Report the malaria status of this cell.
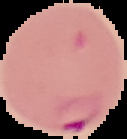
It is parasitized.

preparation: thin blood film
image_type: segmented cell region with the area outside set to black
image_size: 127×139 pixels